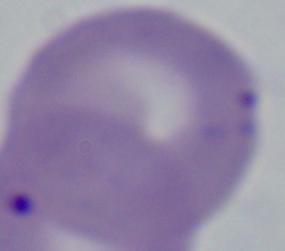

{
  "modality": "photomicrograph",
  "identification": "Babesia",
  "magnification": "1000x"
}